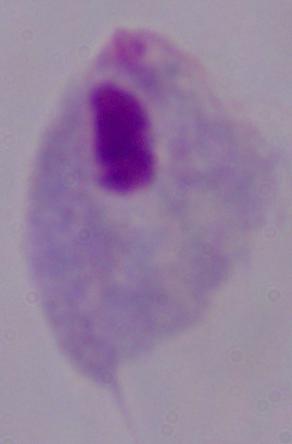
{
  "identification": "trichomonad",
  "modality": "micrograph",
  "magnification": "1000x"
}